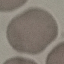
Malaria status: uninfected. Thin blood film. Cell patch, automatically extracted from a larger field of view and resized to 64 × 64 pixels. Photographed with a smartphone camera at the microscope eyepiece. Giemsa-stained preparation.